Locate every blood parasite and identify its species.
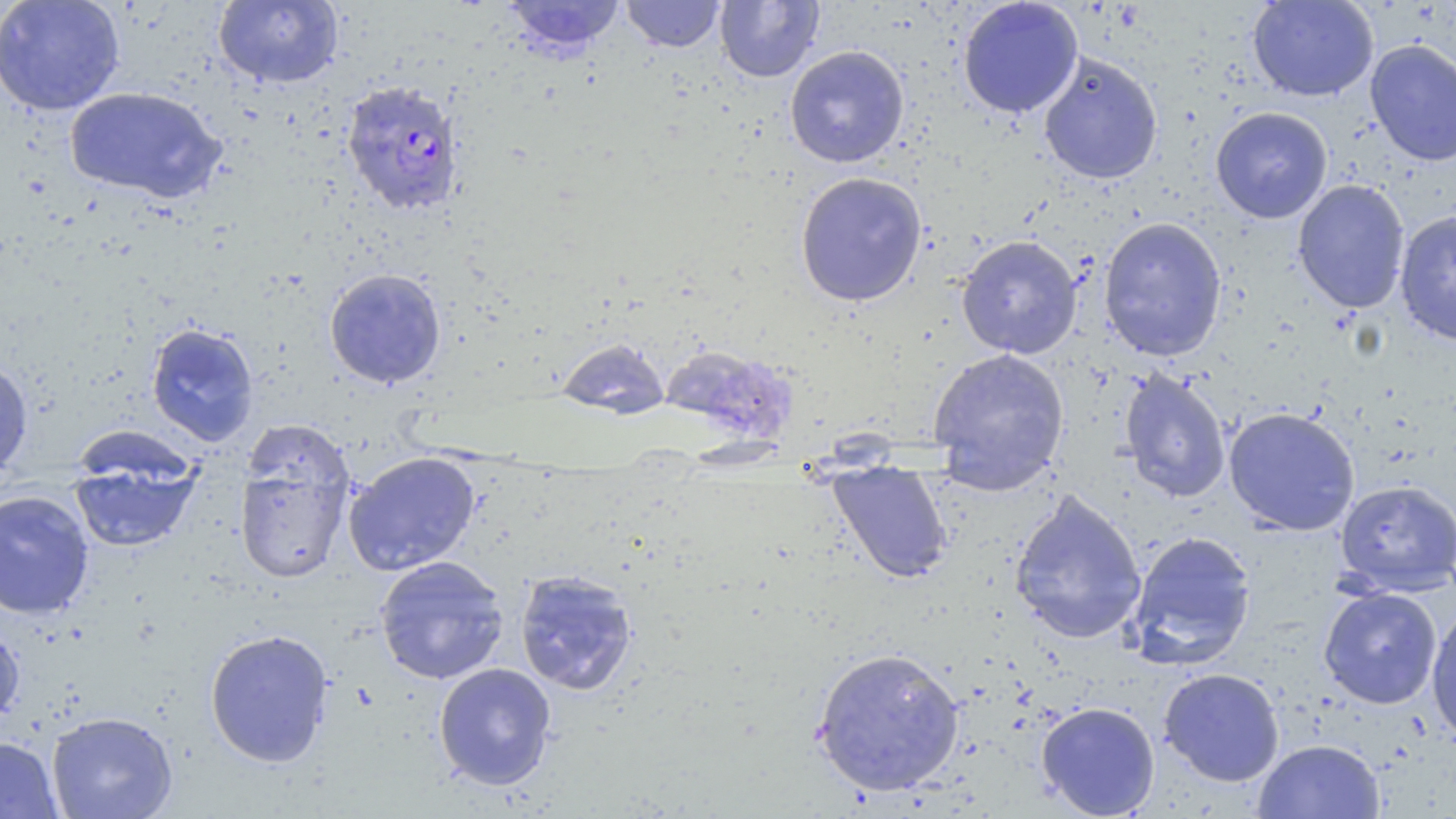

Approximate bounding boxes as (x1,y1)-(x2,y2) corner pairs in pixels.
Plasmodium falciparum-infected red blood cells: (340,79)-(465,216).
No Plasmodium ovale, Plasmodium malariae, Plasmodium vivax, Babesia divergens, or Trypanosoma brucei observed.

Uninfected red blood cell locations: (0,0)-(125,116), (213,0)-(344,88), (499,0)-(627,56), (621,0)-(725,52), (715,0)-(823,82), (958,0)-(1083,118), (1247,0)-(1379,102), (1364,39)-(1456,166), (784,45)-(909,168), (1038,52)-(1163,185), (64,86)-(227,204), (1210,107)-(1332,223), (794,171)-(927,307), (1292,179)-(1411,314), (1394,210)-(1456,345), (1098,216)-(1227,362), (956,234)-(1083,359), (324,268)-(447,389), (146,322)-(259,447), (556,337)-(670,419), (660,344)-(795,445), (927,347)-(1070,486), (0,357)-(33,476), (1118,368)-(1232,504), (1223,406)-(1361,536), (233,433)-(356,587), (343,451)-(482,576), (68,452)-(202,554), (828,462)-(954,583), (1335,479)-(1455,596), (0,490)-(95,620), (1009,490)-(1147,645), (1125,530)-(1257,670), (373,555)-(510,685), (514,569)-(639,696), (1318,586)-(1442,709), (1426,603)-(1456,745), (0,619)-(25,728), (204,628)-(333,767), (811,646)-(965,797), (434,662)-(557,790), (1158,667)-(1285,787), (1036,701)-(1160,818), (46,711)-(178,819), (0,735)-(62,819), (1253,738)-(1384,818). Slide-level diagnosis: Plasmodium falciparum. Thin blood smear. One field of a larger specimen. May-Grünwald-Giemsa stain. Image is 1456×819 pixels. Light microscopy. 1000x magnification.